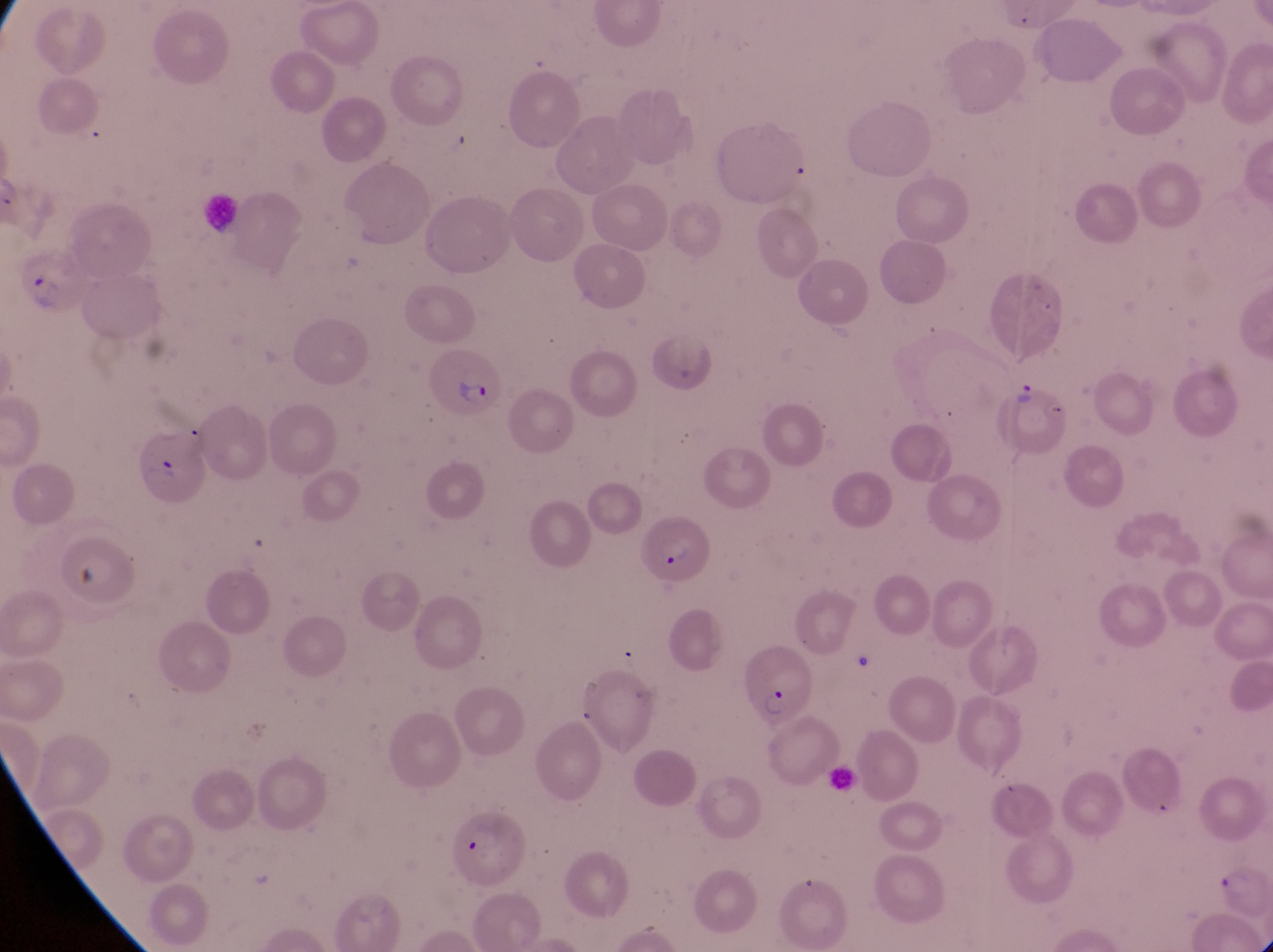
image size = 1273×952 pixels
country = Uganda
magnification = 1000x
field of view = single
capture = smartphone photograph through the eyepiece of an Olympus CX-23 microscope
parasitised red blood cell locations = approximate bounding boxes as (left, top, right, bottom) in pixels: (17, 244, 84, 318), (426, 347, 500, 425), (1001, 379, 1073, 464), (641, 515, 715, 589), (739, 642, 813, 727), (451, 814, 531, 894), (1204, 860, 1269, 932)
artifact (platelet-like body, stain precipitate, or debris) locations = approximate bounding boxes as (left, top, right, bottom) in pixels: (70, 559, 102, 599)
preparation = thin blood smear
leukocyte locations = approximate bounding boxes as (left, top, right, bottom) in pixels: (192, 187, 244, 237)